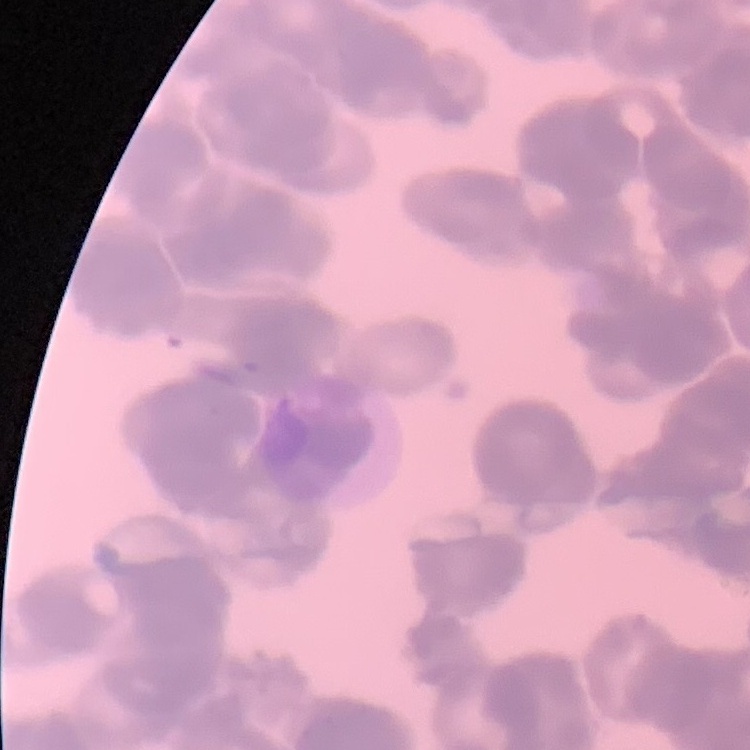
erythrocyte morphology = rouleaux formation
stain = Field's or Giemsa
preparation = thin peripheral smear
image type = square crop of a larger photomicrograph